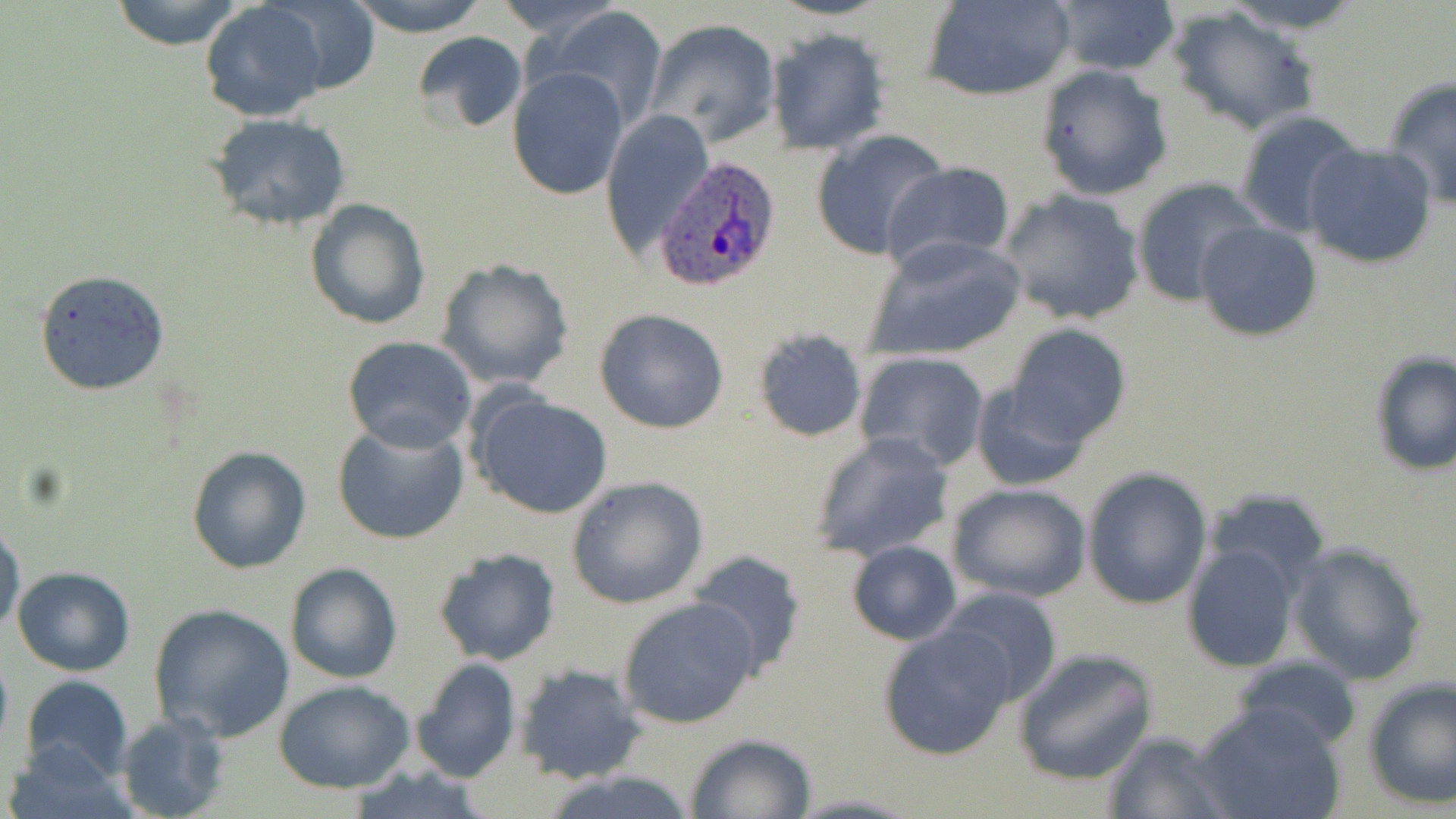
Summary:
  - Coordinate format: approximate bounding boxes as (x1, y1, x2, y2) in pixels
  - Plasmodium ovale-infected red blood cell locations: (655, 156, 783, 292)
  - Uninfected red blood cell locations: (108, 0, 246, 50), (197, 0, 332, 120), (260, 0, 384, 99), (346, 0, 496, 37), (489, 0, 627, 42), (1215, 0, 1372, 33), (924, 1, 1075, 101), (1047, 1, 1180, 78), (1169, 6, 1323, 136), (544, 7, 670, 130), (644, 18, 782, 145), (764, 27, 891, 155), (411, 30, 529, 132), (1036, 64, 1174, 199), (507, 68, 629, 200), (1382, 75, 1456, 210), (601, 109, 714, 261), (1234, 109, 1369, 238), (204, 113, 350, 233), (809, 129, 952, 260), (1303, 142, 1438, 270), (882, 160, 1017, 275), (1130, 177, 1266, 306), (998, 189, 1146, 326), (303, 198, 431, 331), (1195, 220, 1322, 342), (864, 235, 1026, 361), (434, 257, 576, 393), (31, 269, 169, 396), (593, 307, 731, 434), (1003, 324, 1133, 450), (751, 328, 869, 442), (341, 336, 479, 453), (853, 350, 991, 472), (1367, 350, 1456, 478), (968, 376, 1097, 491), (470, 392, 615, 521), (331, 420, 470, 546), (808, 431, 957, 563), (186, 445, 312, 575), (1082, 467, 1212, 611), (566, 476, 710, 610), (947, 482, 1094, 604), (0, 521, 26, 637), (1180, 538, 1303, 675), (846, 540, 962, 645), (1286, 541, 1429, 685), (433, 546, 560, 668), (687, 551, 808, 677), (283, 562, 404, 684), (12, 567, 136, 676), (937, 585, 1063, 709), (617, 595, 761, 730), (147, 602, 297, 743), (878, 623, 1017, 761), (1013, 648, 1156, 786), (1232, 654, 1362, 751), (410, 657, 520, 784), (513, 663, 645, 785), (18, 674, 134, 782), (1362, 678, 1456, 808), (274, 680, 415, 794), (1192, 700, 1347, 819), (115, 710, 231, 819), (1102, 730, 1234, 819), (684, 733, 816, 818), (6, 741, 140, 819), (344, 763, 501, 819), (536, 768, 703, 819), (785, 792, 921, 819)
  - Slide-level diagnosis: Plasmodium ovale
  - Image size: 1456×819 pixels
  - Modality: optical microscopy
  - Stain: May-Grünwald-Giemsa
  - Preparation: thin blood smear
  - Field of view: one of a larger specimen
  - Magnification: 1000x